Describe the morphology of the red blood cells.
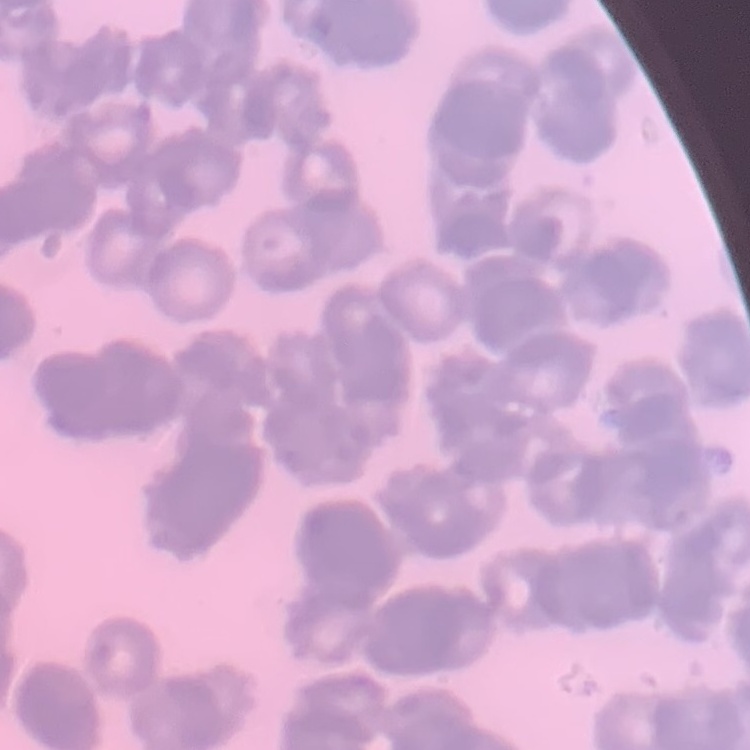
They show rouleaux formation.

Thin blood film. Square crop of a larger photomicrograph. Field's or Giemsa stain.